State the blood parasite species.
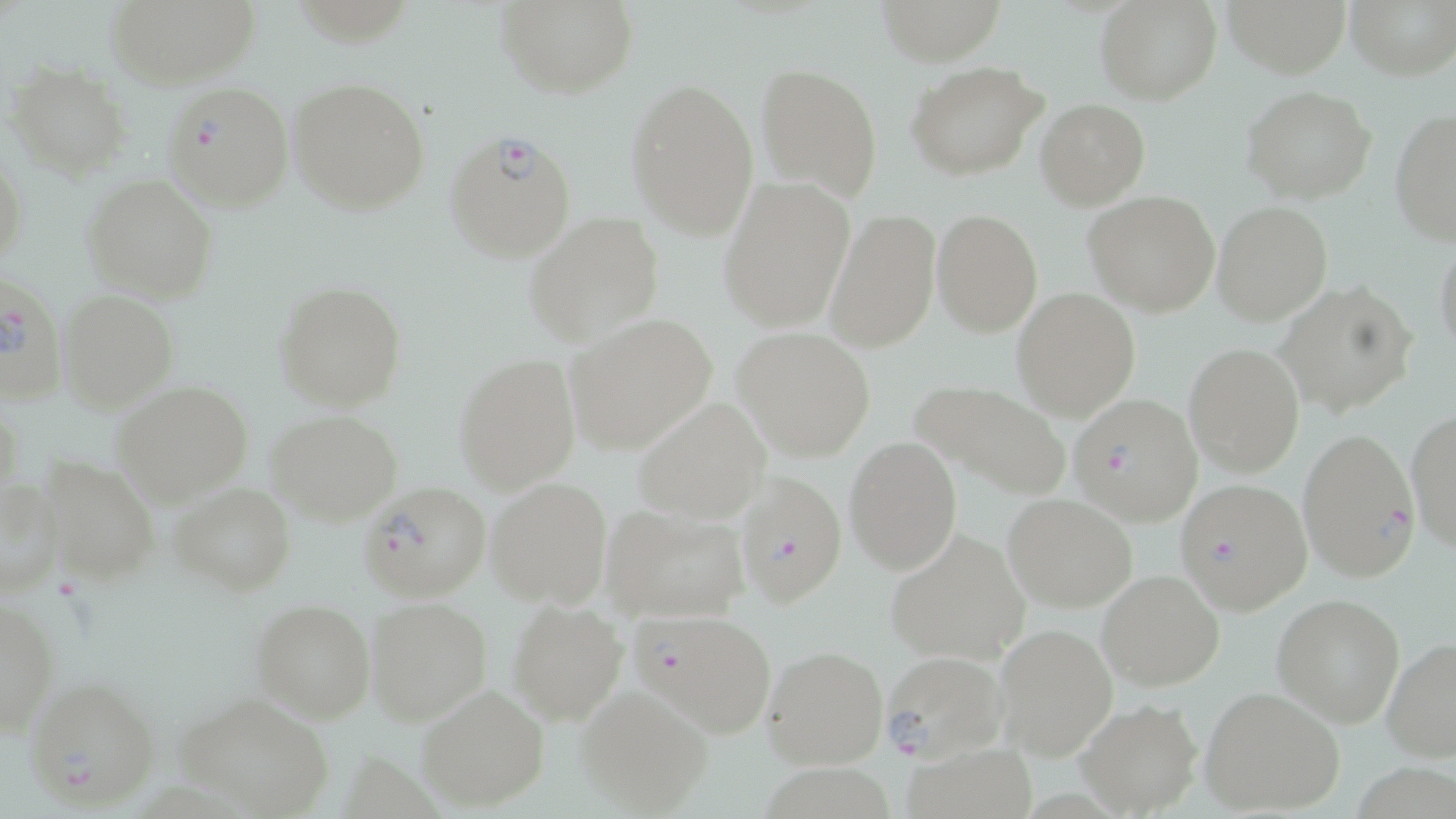

Plasmodium falciparum.

Summary:
  - Coordinate format: approximate bounding boxes as (x1, y1, x2, y2) in pixels
  - Plasmodium falciparum-infected red blood cell locations: (162, 80, 296, 211), (443, 128, 577, 263), (0, 268, 65, 406), (1068, 394, 1204, 525), (1299, 428, 1421, 581), (733, 471, 847, 609), (1175, 478, 1313, 613), (358, 482, 490, 603), (631, 606, 781, 743), (877, 650, 1008, 763), (24, 676, 162, 812)
  - Uninfected red blood cell locations: (104, 0, 261, 88), (495, 0, 637, 96), (871, 0, 1011, 65), (1095, 0, 1222, 105), (1221, 0, 1354, 76), (1346, 0, 1456, 81), (905, 61, 1048, 181), (756, 63, 884, 201), (7, 65, 130, 179), (289, 77, 432, 216), (625, 78, 759, 239), (1241, 87, 1377, 204), (1036, 98, 1149, 209), (1389, 107, 1456, 245), (0, 150, 24, 273), (81, 175, 220, 303), (718, 175, 855, 333), (1084, 191, 1222, 316), (1212, 201, 1333, 324), (824, 207, 940, 353), (932, 208, 1043, 336), (524, 213, 665, 346), (1434, 237, 1456, 360), (274, 280, 407, 411), (1276, 280, 1418, 418), (57, 289, 179, 413), (1012, 289, 1139, 420), (563, 314, 719, 455), (731, 327, 876, 461), (1185, 342, 1305, 476), (453, 354, 581, 493), (911, 379, 1071, 500), (113, 380, 253, 507), (632, 395, 771, 525), (1404, 408, 1456, 553), (266, 410, 404, 526), (844, 436, 962, 575), (36, 454, 159, 587), (0, 476, 64, 598), (486, 476, 614, 609), (172, 482, 297, 596), (1002, 493, 1138, 612), (601, 504, 750, 624), (883, 528, 1029, 663), (1097, 570, 1225, 693), (1271, 591, 1405, 729), (0, 595, 59, 738), (364, 597, 492, 726), (506, 598, 628, 724), (250, 599, 376, 722), (993, 623, 1118, 761), (1382, 636, 1456, 762), (762, 645, 891, 772), (416, 683, 551, 810), (1201, 686, 1347, 817), (575, 687, 712, 816), (173, 689, 336, 819), (1076, 699, 1203, 816), (903, 740, 1035, 819)
  - Stain: May-Grünwald-Giemsa
  - Preparation: thin blood smear
  - Magnification: 1000x
  - Field of view: single
  - Image size: 1456×819 pixels
  - Modality: light microscopy